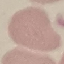
Summary:
  - Result: negative for malaria parasites
  - Image type: automatically extracted cell patch, resized to 64 × 64 pixels
  - Preparation: thin blood smear
  - Stain: Giemsa
  - Capture: smartphone camera at the microscope eyepiece